State which cell type is depicted.
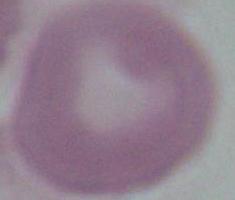

An erythrocyte.

Summary:
  - Modality: micrograph
  - Magnification: 1000x